Assess this cell for malaria.
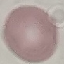

It is uninfected.

Thin blood film. Automatically extracted cell patch, resized to 64 × 64 pixels. Photographed with a smartphone camera at the microscope eyepiece. Giemsa-stained preparation.